Comment on the morphology of the erythrocytes.
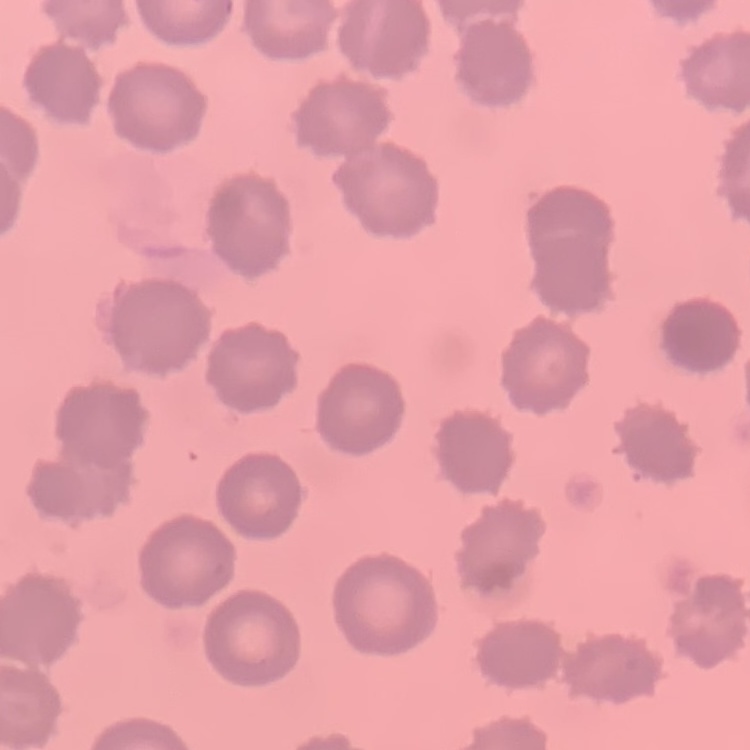

No rouleaux formation.

One tile cut from a larger photomicrograph. Stained with either Field's or Giemsa. Thin blood film.